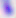
Summary:
  - Magnification: 400x
  - Identification: Toxoplasma gondii
  - Modality: photomicrograph